Report the malaria status of this cell.
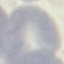

Uninfected.

Automatically extracted cell patch, resized to 64 × 64 pixels. Giemsa-stained preparation. Thin smear of blood. Photographed with a smartphone camera at the microscope eyepiece.